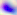 Toxoplasma gondii is seen. Micrograph. 400x magnification.